Locate every leukocyte (white blood cell).
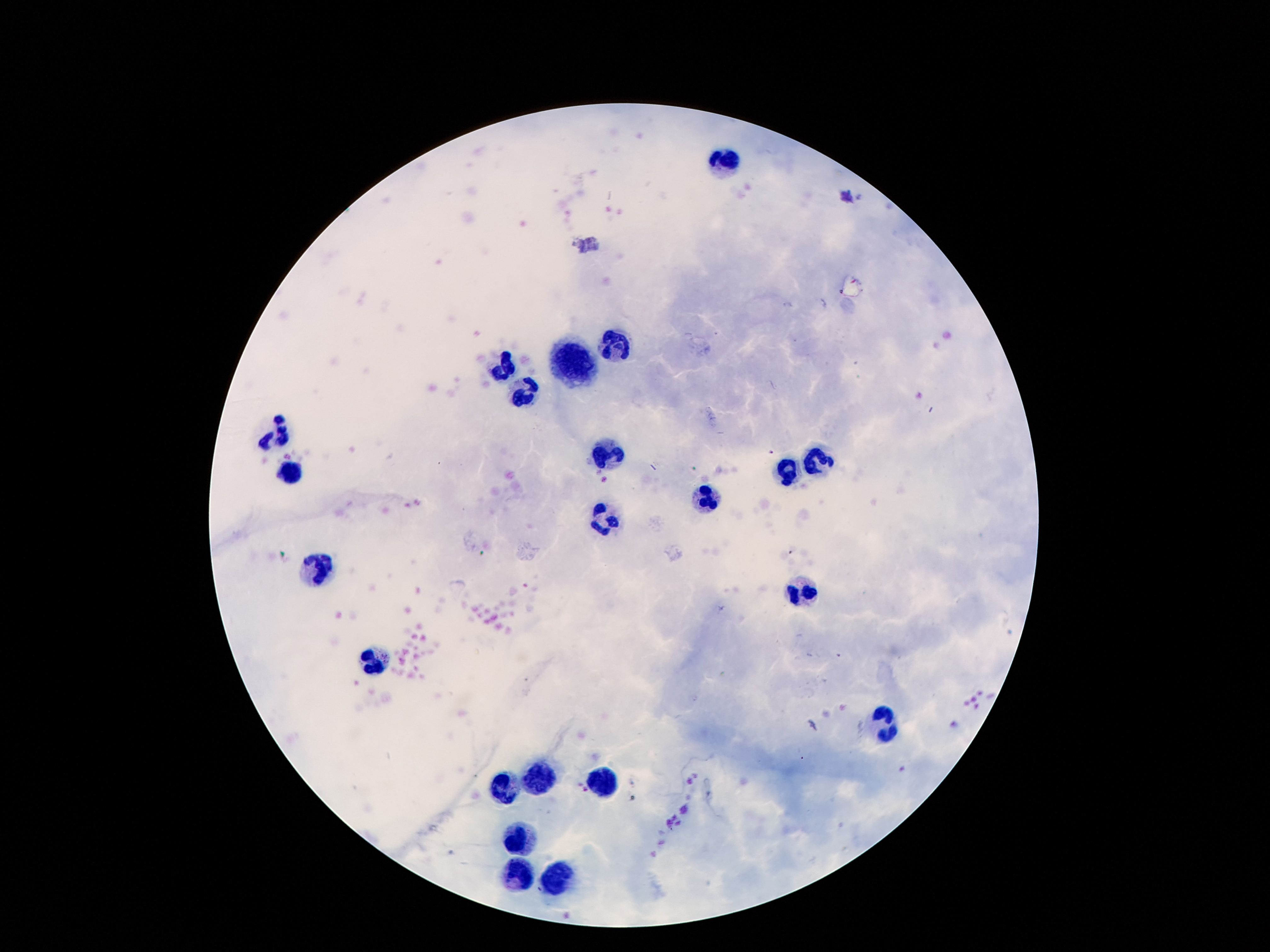
Approximate centers as {x, y} in pixels.
Leukocytes: {725, 160}, {620, 345}, {574, 363}, {507, 367}, {528, 395}, {280, 433}, {820, 458}, {608, 461}, {295, 473}, {788, 473}, {704, 496}, {604, 525}, {316, 566}, {799, 588}, {373, 662}, {885, 723}, {538, 779}, {604, 784}, {505, 788}, {524, 844}, {513, 876}, {553, 880}.

Image is 1270×952 pixels. 100x magnification. Smartphone photograph taken through the microscope eyepiece. Patient malaria status: negative. One field from this slide. Thick blood film. Giemsa-stained preparation.